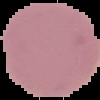
Summary:
  - Preparation: thin blood film
  - Image size: 100×100 pixels
  - Image type: segmented cell region with the area outside set to black
  - Result: no malaria parasites seen